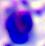
magnification = 400x
identification = white blood cell
modality = micrograph